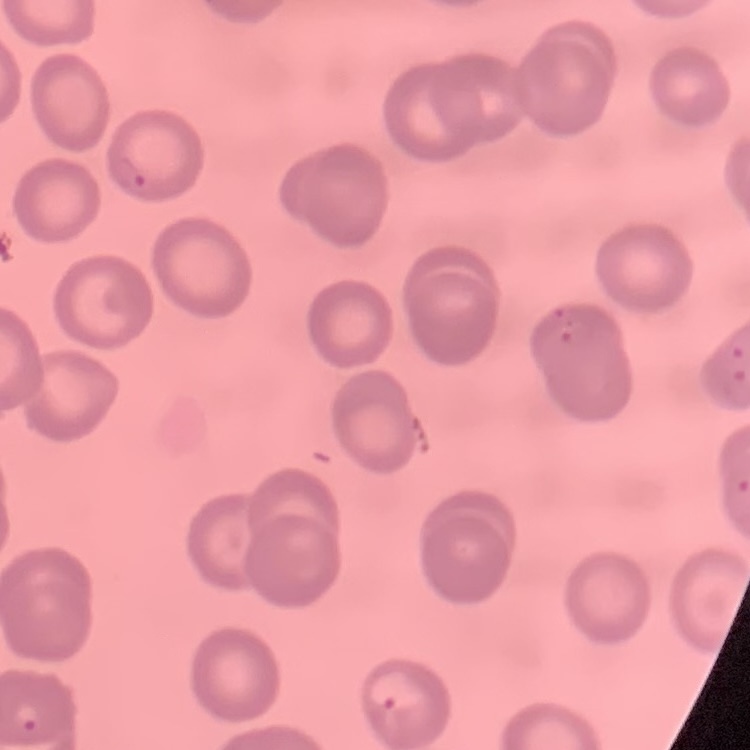
red blood cell morphology = no rouleaux formation
image type = square crop of a larger photomicrograph
stain = Field's or Giemsa
preparation = thin blood smear